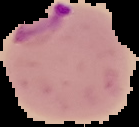
preparation = thin blood film
malaria status = parasitized
image type = segmented cell region on a black background
image size = 139×127 pixels